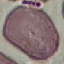
{
  "result": "negative for malaria parasites",
  "stain": "Giemsa",
  "preparation": "thin smear",
  "image_type": "cell patch, automatically extracted from a larger field of view and resized to 64 × 64 pixels",
  "capture": "smartphone through the microscope eyepiece"
}